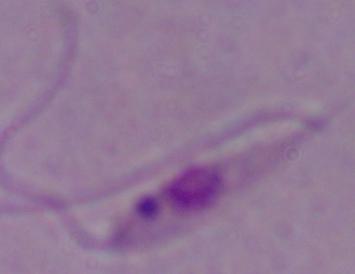
Summary:
  - Identification: Leishmania
  - Magnification: 1000x
  - Modality: micrograph